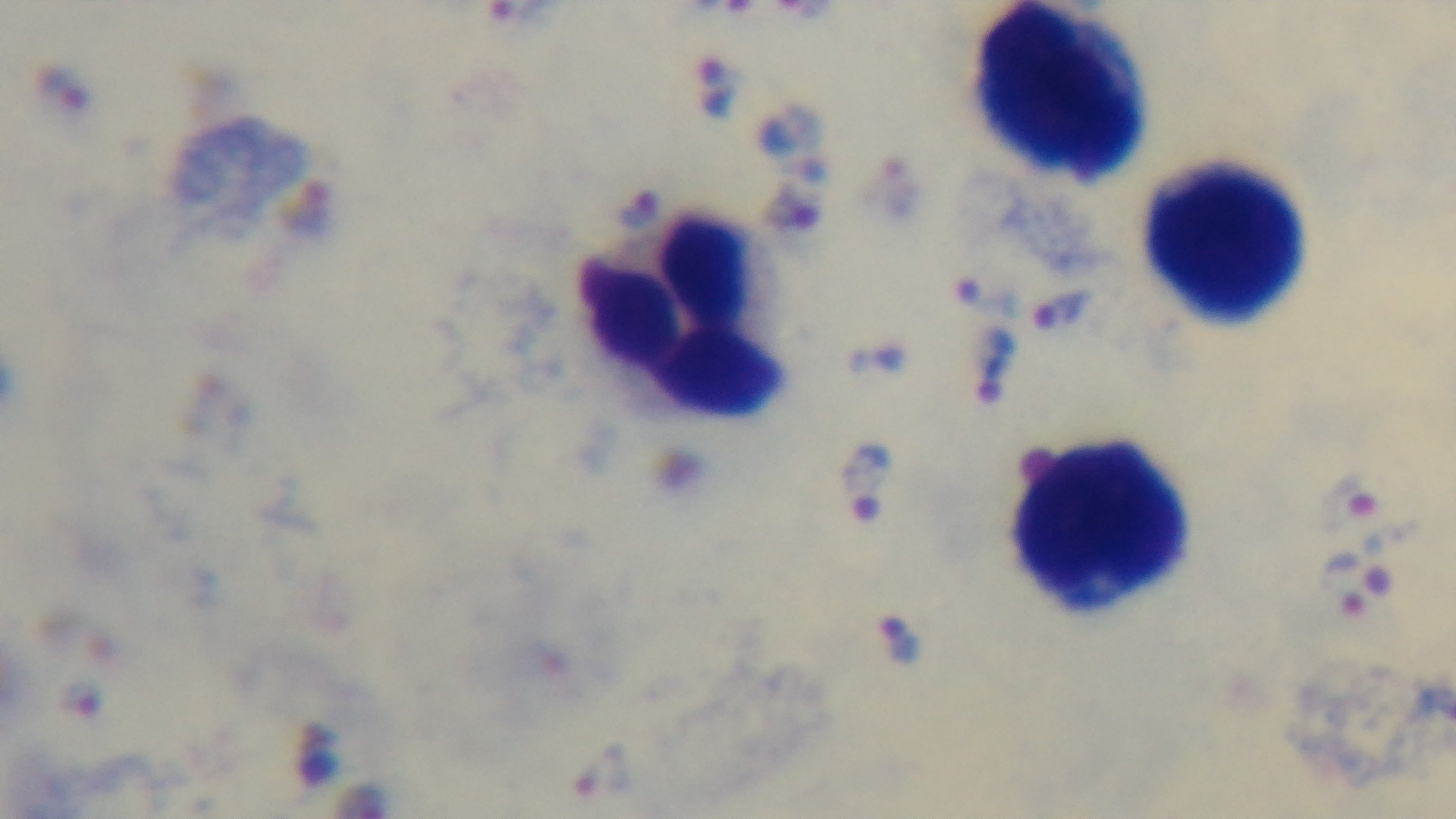
100x oil-immersion objective. Malaria status: infected. Photomicrograph. Preparation: thick smear. One field from the slide. Giemsa stain. Captured with a mounted 4K digital camera.